Mark where leukocytes are.
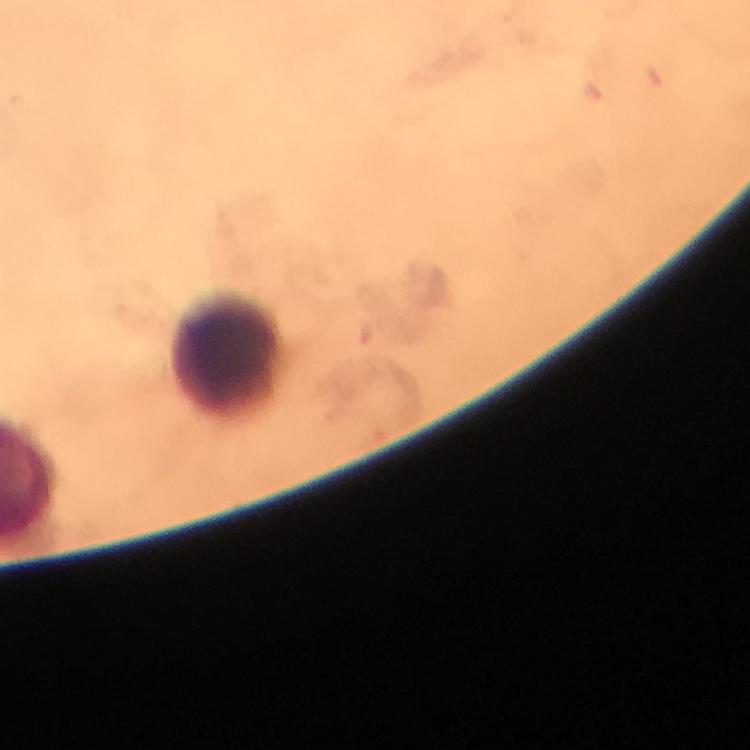
Approximate centers as (x, y) in pixels.
Leukocytes: (230, 358).

context = from a malaria diagnostic workup
cropped from = one field of view
capture = smartphone camera through the microscope
image size = 750×750 pixels
preparation = thick blood film
Plasmodium parasites = none detected
magnification = 100x
immersion oil = used
stain = Giemsa